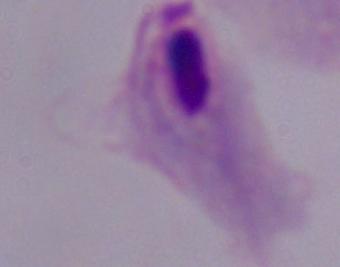

Captured at 1000x magnification. Micrograph. A trichomonad is seen.